Outline each uninfected red blood cell.
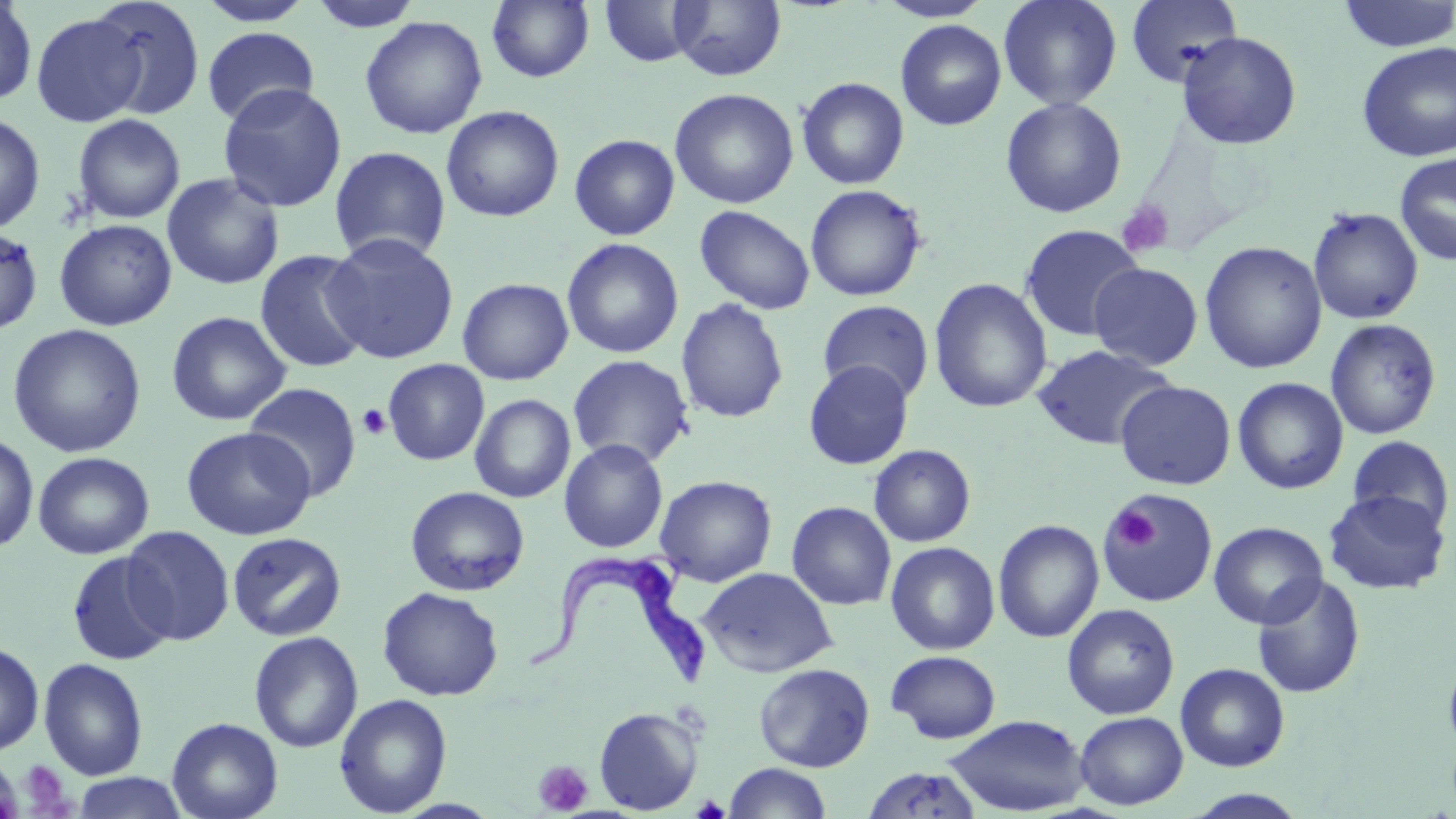

Approximate bounding boxes as (x1, y1, x2, y2) in pixels.
Uninfected red blood cells: (86, 0, 206, 121), (196, 0, 316, 27), (307, 0, 424, 32), (669, 0, 787, 81), (876, 0, 994, 22), (998, 0, 1122, 111), (1125, 0, 1243, 89), (1336, 0, 1456, 53), (0, 1, 38, 107), (487, 1, 595, 83), (600, 1, 703, 67), (30, 12, 148, 127), (359, 15, 488, 139), (896, 19, 1007, 131), (202, 27, 320, 127), (1176, 31, 1302, 150), (1356, 42, 1456, 162), (796, 77, 910, 190), (217, 82, 347, 213), (669, 87, 799, 209), (1000, 97, 1127, 218), (441, 105, 565, 223), (0, 112, 45, 234), (72, 113, 186, 224), (569, 134, 680, 240), (329, 146, 451, 264), (1394, 152, 1456, 266), (161, 173, 285, 290), (805, 184, 927, 302), (695, 205, 816, 314), (1307, 207, 1424, 325), (54, 219, 177, 331), (1019, 224, 1144, 342), (0, 226, 44, 336), (322, 232, 460, 365), (562, 237, 684, 359), (1199, 241, 1327, 374), (254, 249, 372, 374), (1089, 262, 1203, 370), (457, 277, 574, 385), (929, 278, 1052, 414), (675, 298, 790, 424), (818, 300, 934, 403), (166, 311, 292, 426), (1324, 318, 1442, 440), (7, 323, 147, 458), (1031, 343, 1176, 450), (567, 354, 695, 469), (383, 359, 489, 465), (803, 360, 915, 469), (1232, 377, 1348, 494), (1115, 380, 1237, 490), (244, 382, 362, 501), (469, 394, 576, 503), (181, 426, 316, 540), (0, 433, 39, 553), (1346, 435, 1455, 533), (559, 439, 668, 553), (868, 444, 976, 547), (33, 451, 154, 559), (655, 475, 778, 586), (405, 486, 530, 596), (1323, 489, 1451, 594), (1101, 490, 1218, 608), (787, 501, 896, 610), (993, 519, 1104, 643), (1209, 521, 1328, 628), (121, 526, 235, 645), (227, 531, 347, 641), (885, 541, 1000, 654), (66, 551, 175, 666), (699, 566, 838, 677), (1251, 574, 1365, 698), (377, 586, 504, 701), (1062, 603, 1179, 720), (249, 631, 363, 752), (0, 641, 44, 756), (1442, 647, 1456, 760), (886, 650, 1001, 743), (39, 657, 148, 780), (753, 662, 875, 772), (1175, 662, 1291, 772), (334, 693, 452, 817), (594, 706, 703, 814), (1074, 711, 1188, 810), (942, 714, 1090, 816), (166, 717, 283, 819), (723, 763, 833, 819), (861, 766, 983, 818), (72, 773, 189, 818), (1183, 788, 1310, 818).

slide_level_diagnosis: Trypanosoma brucei
preparation: thin blood smear
stain: May-Grünwald-Giemsa
platelet_locations: 'approximate bounding boxes as (x1, y1, x2, y2) in pixels: (1117, 200, 1175, 258), (357, 404, 392, 440), (1110, 509, 1158, 551), (0, 758, 24, 819), (18, 760, 71, 814), (534, 760, 593, 815)'
field_of_view: one of a larger specimen
image_size: 1456×819 pixels
magnification: 1000x
modality: light microscopy
trypanosoma_brucei_locations: 'approximate bounding boxes as (x1, y1, x2, y2) in pixels: (526, 549, 711, 696)'